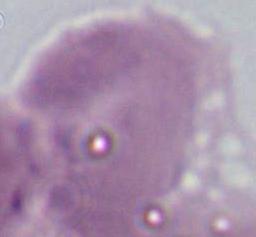 A red blood cell is seen. Photomicrograph. 1000x magnification.